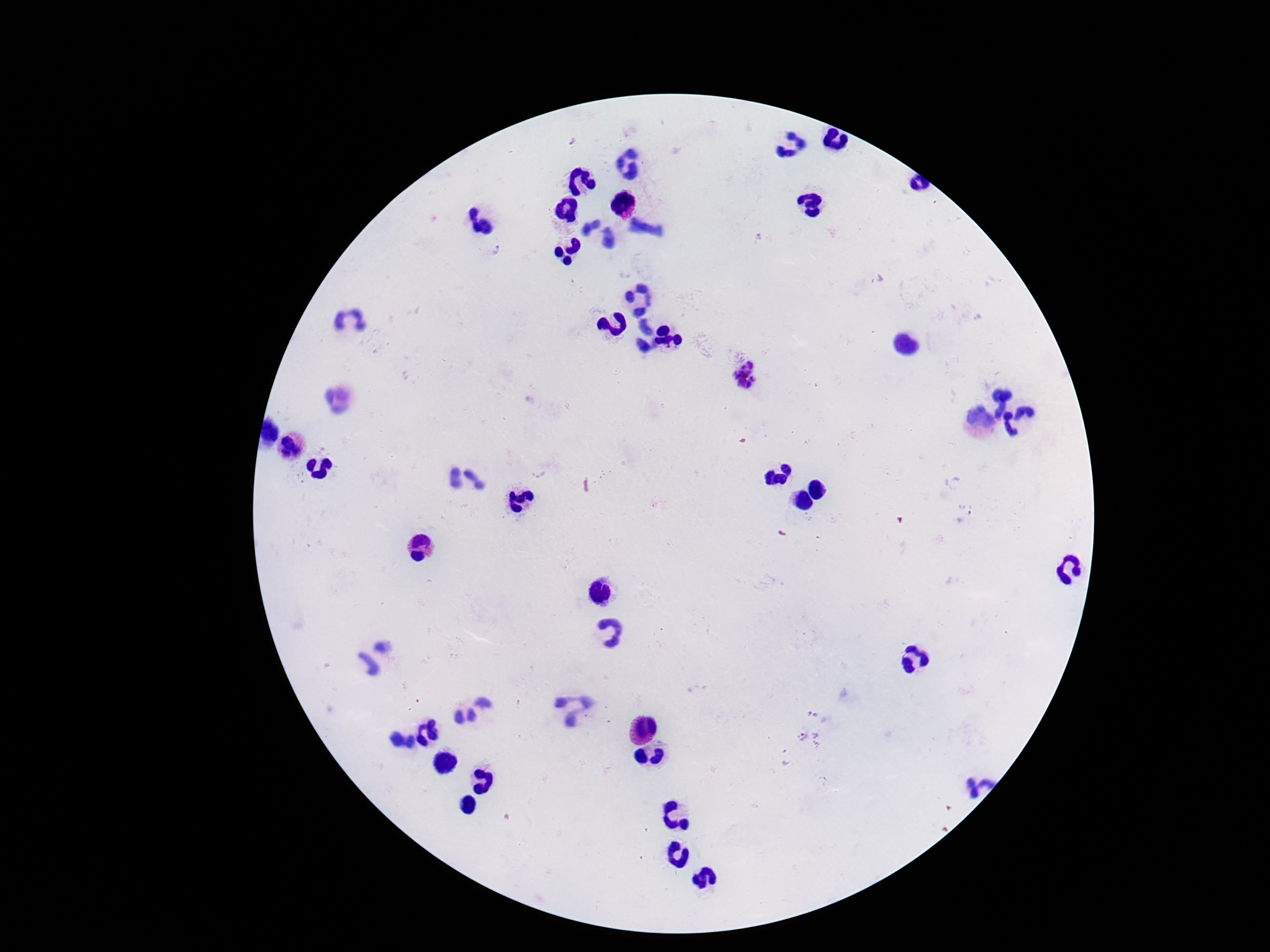 Approximate centers as [x, y] in pixels. Plasmodium parasite locations: [572, 139], [495, 250], [746, 375], [966, 504], [815, 712], [810, 740], [785, 758]. One field from this slide. 100x magnification. Smartphone photograph taken through the microscope eyepiece. Giemsa-stained preparation. Image is 1270×952 pixels. Patient malaria status: positive. Thick peripheral-blood smear.